Outline each Plasmodium ovale-infected red blood cell.
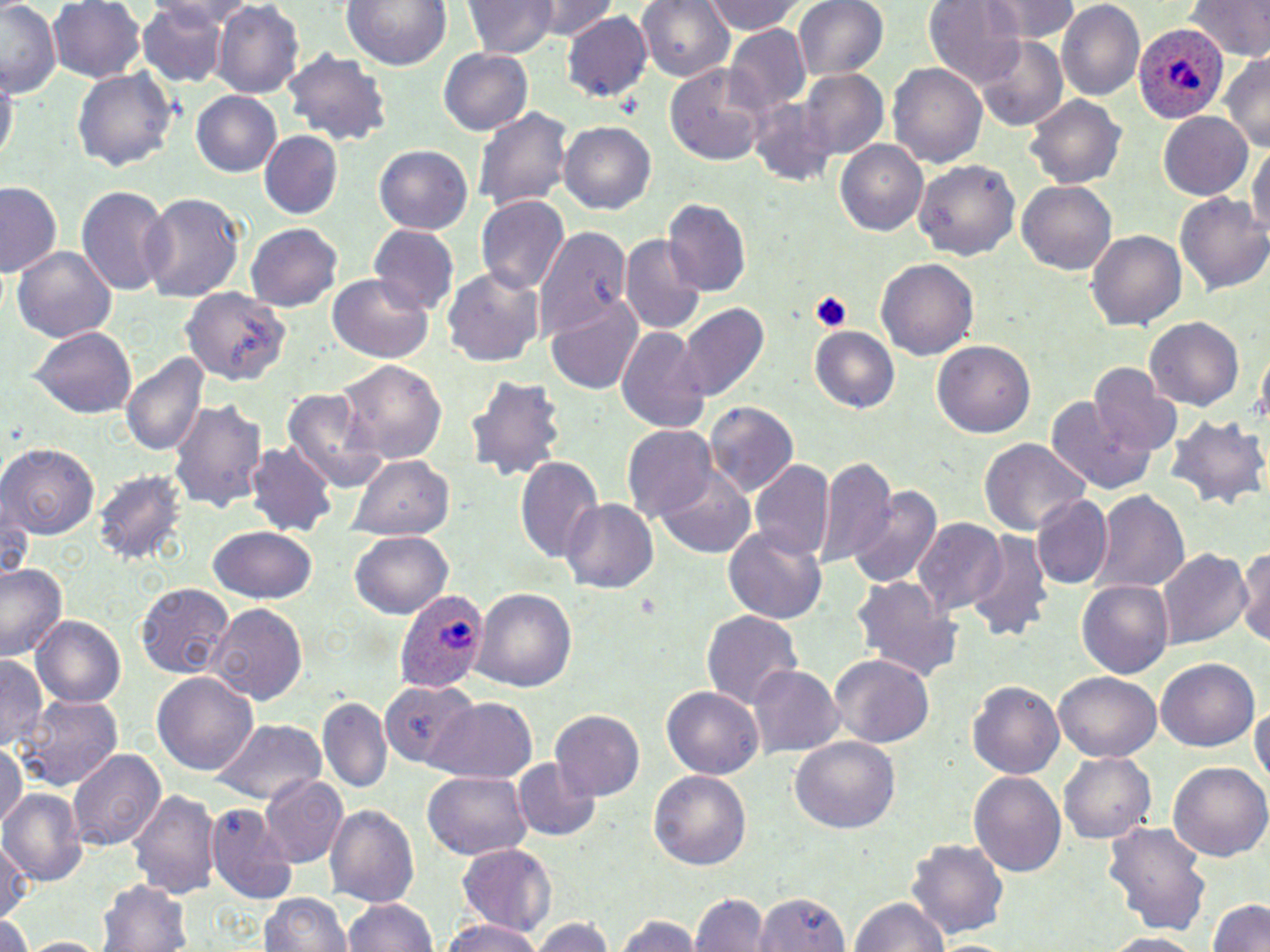

Approximate bounding boxes as named x1/y1/x2/y2 corners in pixels.
Plasmodium ovale-infected red blood cells: (x1=1131, y1=25, x2=1227, y2=124), (x1=395, y1=586, x2=488, y2=696).

Summary:
  - Platelet locations: (x1=809, y1=289, x2=850, y2=333)
  - Uninfected red blood cell locations: (x1=50, y1=0, x2=148, y2=85), (x1=344, y1=0, x2=450, y2=71), (x1=465, y1=0, x2=556, y2=60), (x1=535, y1=0, x2=611, y2=40), (x1=638, y1=0, x2=735, y2=83), (x1=705, y1=0, x2=802, y2=35), (x1=793, y1=0, x2=890, y2=81), (x1=925, y1=0, x2=1029, y2=89), (x1=985, y1=0, x2=1083, y2=42), (x1=1186, y1=0, x2=1269, y2=62), (x1=136, y1=1, x2=233, y2=89), (x1=213, y1=1, x2=304, y2=99), (x1=1057, y1=2, x2=1144, y2=103), (x1=1, y1=3, x2=64, y2=97), (x1=565, y1=12, x2=652, y2=105), (x1=725, y1=25, x2=813, y2=119), (x1=976, y1=33, x2=1068, y2=131), (x1=285, y1=47, x2=391, y2=149), (x1=438, y1=47, x2=533, y2=135), (x1=1223, y1=55, x2=1270, y2=151), (x1=665, y1=63, x2=770, y2=166), (x1=889, y1=64, x2=986, y2=166), (x1=1, y1=65, x2=16, y2=169), (x1=72, y1=67, x2=177, y2=175), (x1=801, y1=70, x2=888, y2=160), (x1=193, y1=90, x2=283, y2=179), (x1=1024, y1=94, x2=1127, y2=187), (x1=749, y1=96, x2=840, y2=187), (x1=474, y1=106, x2=572, y2=213), (x1=1158, y1=112, x2=1255, y2=200), (x1=561, y1=122, x2=656, y2=216), (x1=259, y1=132, x2=341, y2=217), (x1=835, y1=139, x2=928, y2=238), (x1=1248, y1=141, x2=1270, y2=247), (x1=374, y1=145, x2=473, y2=235), (x1=914, y1=158, x2=1022, y2=262), (x1=0, y1=181, x2=63, y2=277), (x1=1017, y1=182, x2=1117, y2=275), (x1=76, y1=185, x2=172, y2=294), (x1=139, y1=191, x2=248, y2=302), (x1=1175, y1=191, x2=1270, y2=296), (x1=478, y1=197, x2=568, y2=296), (x1=663, y1=199, x2=750, y2=298), (x1=246, y1=224, x2=342, y2=312), (x1=533, y1=225, x2=631, y2=345), (x1=371, y1=227, x2=457, y2=313), (x1=1087, y1=229, x2=1184, y2=333), (x1=619, y1=234, x2=704, y2=335), (x1=14, y1=245, x2=116, y2=344), (x1=876, y1=258, x2=978, y2=362), (x1=442, y1=269, x2=544, y2=366), (x1=325, y1=274, x2=436, y2=362), (x1=180, y1=291, x2=286, y2=382), (x1=547, y1=295, x2=643, y2=397), (x1=678, y1=301, x2=769, y2=402), (x1=1146, y1=319, x2=1243, y2=409), (x1=615, y1=325, x2=709, y2=435), (x1=808, y1=325, x2=902, y2=415), (x1=31, y1=327, x2=137, y2=418), (x1=934, y1=339, x2=1038, y2=438), (x1=120, y1=350, x2=209, y2=457), (x1=333, y1=358, x2=447, y2=463), (x1=1090, y1=364, x2=1179, y2=456), (x1=466, y1=373, x2=569, y2=483), (x1=282, y1=387, x2=390, y2=491), (x1=1049, y1=394, x2=1159, y2=495), (x1=168, y1=399, x2=268, y2=516), (x1=705, y1=400, x2=799, y2=499), (x1=1167, y1=415, x2=1270, y2=513), (x1=624, y1=426, x2=719, y2=520), (x1=979, y1=439, x2=1086, y2=535), (x1=248, y1=443, x2=340, y2=539), (x1=2, y1=444, x2=98, y2=537), (x1=516, y1=453, x2=603, y2=564), (x1=349, y1=457, x2=454, y2=539), (x1=813, y1=457, x2=897, y2=566), (x1=749, y1=461, x2=834, y2=563), (x1=656, y1=467, x2=756, y2=558), (x1=94, y1=470, x2=186, y2=567), (x1=845, y1=482, x2=943, y2=592), (x1=1093, y1=487, x2=1190, y2=594), (x1=1030, y1=494, x2=1113, y2=589), (x1=561, y1=497, x2=658, y2=596), (x1=2, y1=500, x2=37, y2=583), (x1=914, y1=519, x2=1006, y2=618), (x1=723, y1=525, x2=828, y2=625), (x1=209, y1=526, x2=319, y2=603), (x1=351, y1=531, x2=453, y2=618), (x1=963, y1=531, x2=1054, y2=642), (x1=1239, y1=541, x2=1270, y2=650), (x1=1157, y1=548, x2=1249, y2=650), (x1=0, y1=560, x2=69, y2=661), (x1=851, y1=576, x2=962, y2=679), (x1=1077, y1=578, x2=1173, y2=681), (x1=137, y1=582, x2=236, y2=677), (x1=473, y1=589, x2=577, y2=691), (x1=206, y1=603, x2=309, y2=705), (x1=701, y1=609, x2=802, y2=711), (x1=34, y1=615, x2=127, y2=706), (x1=828, y1=653, x2=934, y2=748), (x1=1, y1=657, x2=47, y2=752), (x1=1157, y1=657, x2=1258, y2=752), (x1=751, y1=664, x2=845, y2=757), (x1=1053, y1=669, x2=1160, y2=761), (x1=154, y1=672, x2=258, y2=777), (x1=966, y1=678, x2=1063, y2=778), (x1=380, y1=680, x2=478, y2=768), (x1=662, y1=687, x2=762, y2=779), (x1=21, y1=695, x2=120, y2=791), (x1=318, y1=696, x2=391, y2=792), (x1=1251, y1=696, x2=1269, y2=801), (x1=429, y1=701, x2=536, y2=786), (x1=550, y1=709, x2=644, y2=797), (x1=212, y1=718, x2=327, y2=803), (x1=791, y1=737, x2=900, y2=833), (x1=0, y1=742, x2=26, y2=829), (x1=68, y1=746, x2=165, y2=852), (x1=1058, y1=750, x2=1155, y2=846), (x1=1167, y1=759, x2=1270, y2=863), (x1=513, y1=760, x2=600, y2=842), (x1=648, y1=768, x2=751, y2=872), (x1=969, y1=769, x2=1067, y2=878), (x1=422, y1=770, x2=532, y2=861), (x1=261, y1=774, x2=348, y2=868), (x1=2, y1=789, x2=85, y2=886), (x1=128, y1=790, x2=218, y2=899), (x1=324, y1=802, x2=420, y2=907), (x1=203, y1=805, x2=294, y2=903), (x1=1102, y1=819, x2=1210, y2=935), (x1=908, y1=835, x2=1009, y2=942), (x1=0, y1=839, x2=32, y2=930), (x1=455, y1=844, x2=554, y2=934), (x1=101, y1=878, x2=192, y2=952), (x1=693, y1=890, x2=767, y2=952), (x1=750, y1=891, x2=855, y2=952), (x1=260, y1=892, x2=352, y2=952), (x1=342, y1=897, x2=437, y2=952), (x1=850, y1=897, x2=949, y2=952), (x1=1208, y1=897, x2=1270, y2=952), (x1=615, y1=910, x2=702, y2=951), (x1=0, y1=916, x2=33, y2=952), (x1=531, y1=916, x2=613, y2=952), (x1=440, y1=917, x2=543, y2=951), (x1=1094, y1=933, x2=1212, y2=951), (x1=15, y1=936, x2=110, y2=952)
  - Slide-level diagnosis: Plasmodium ovale
  - Preparation: thin blood film
  - Image size: 1270×952 pixels
  - Modality: light microscopy
  - Stain: May-Grünwald-Giemsa
  - Magnification: 1000x
  - Field of view: single